Report the malaria status of this cell.
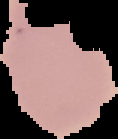

It is parasitized.

preparation = thin blood film
image type = cell region segmented out of the field of view; surrounding area masked to black
image size = 118×139 pixels